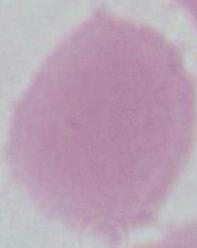
modality: photomicrograph
magnification: 1000x
identification: erythrocyte